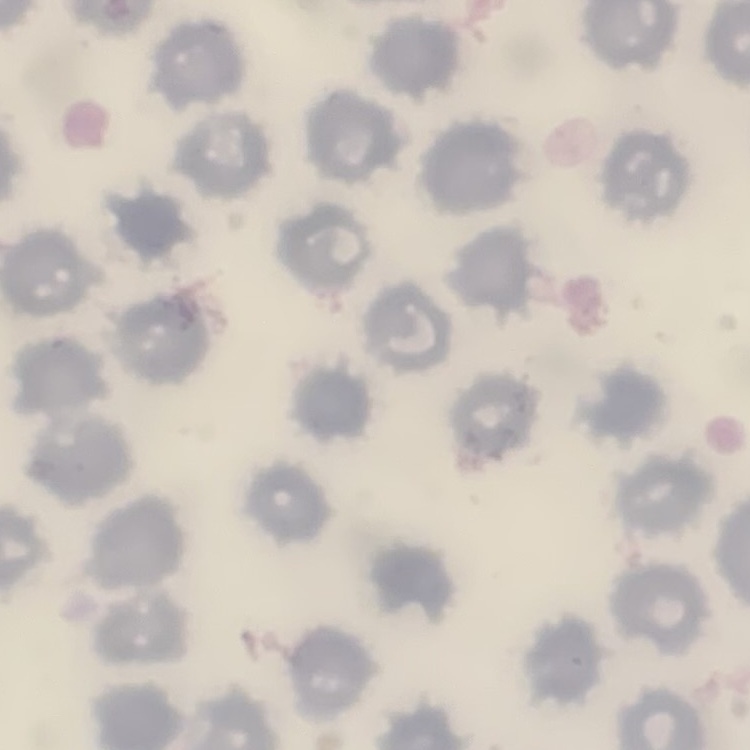

red blood cell morphology = no rouleaux formation
stain = Field's or Giemsa
image type = one tile cut from a larger photomicrograph
preparation = thin blood film